Locate every Plasmodium falciparum-infected red blood cell.
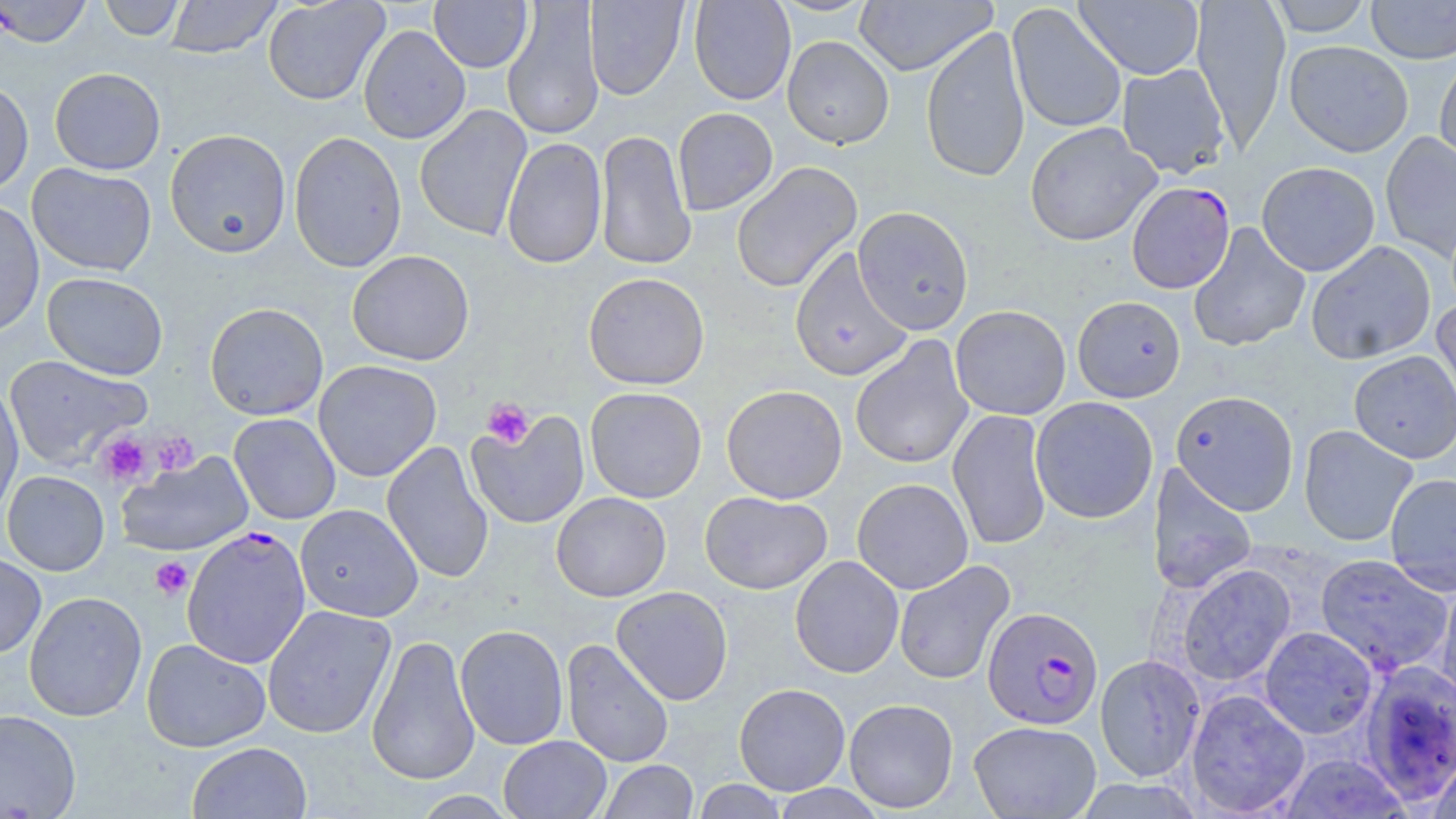
Approximate bounding boxes as (x1,y1)-(x2,y2) corner pairs in pixels.
Plasmodium falciparum-infected red blood cells (subset): (1126,181)-(1235,294), (182,526)-(312,668), (982,606)-(1104,729).

{
  "slide_level_diagnosis": "Plasmodium falciparum",
  "stain": "May-Grünwald-Giemsa",
  "preparation": "thin blood smear",
  "platelet_locations": "approximate bounding boxes as (x1,y1)-(x2,y2) corner pairs in pixels: (483,398)-(534,449), (151,431)-(199,475), (97,432)-(153,487), (149,556)-(193,601)",
  "field_of_view": "single",
  "modality": "optical microscopy",
  "uninfected_red_blood_cell_locations_subset": "approximate bounding boxes as (x1,y1)-(x2,y2) corner pairs in pixels: (99,0)-(185,41), (164,0)-(282,58), (262,0)-(389,106), (429,0)-(533,73), (689,0)-(796,105), (769,0)-(879,17), (853,0)-(997,76), (1074,0)-(1205,80), (1192,0)-(1291,151), (1267,0)-(1373,37), (1365,0)-(1456,63), (501,1)-(605,140), (585,1)-(688,100), (1007,3)-(1127,134), (358,25)-(470,144), (921,26)-(1030,183), (782,36)-(894,149), (1284,40)-(1414,157), (1435,54)-(1456,170), (1116,63)-(1230,179), (49,67)-(166,175), (0,79)-(34,197), (415,104)-(532,242), (673,107)-(778,215), (1024,123)-(1160,246), (165,129)-(291,258), (595,129)-(696,270), (288,131)-(407,273), (1380,131)-(1456,262), (501,137)-(607,269), (1256,161)-(1380,277), (27,162)-(156,276), (731,162)-(863,293), (0,199)-(45,338), (853,206)-(974,335), (1187,222)-(1311,352), (1306,240)-(1436,365), (789,246)-(914,382), (347,250)-(475,366), (42,272)-(168,380), (583,272)-(710,390), (1072,295)-(1186,402), (1431,297)-(1456,426), (204,302)-(329,420), (950,305)-(1071,420), (850,336)-(974,470), (1349,350)-(1456,464), (3,355)-(152,471), (313,360)-(442,482), (0,384)-(23,520), (721,385)-(847,504), (585,387)-(707,503), (1170,390)-(1299,515), (1030,396)-(1158,524), (465,409)-(590,529), (947,409)-(1052,551), (229,413)-(341,524), (1298,424)-(1418,547), (382,441)-(494,584), (116,452)-(254,557), (1147,464)-(1258,596), (1,470)-(110,576), (1384,473)-(1456,595), (852,478)-(973,594), (699,491)-(832,595), (551,492)-(671,602), (295,504)-(422,621), (0,551)-(47,659), (1315,553)-(1455,678), (789,556)-(904,679), (893,560)-(1016,686), (1175,564)-(1296,687), (1434,577)-(1456,711), (611,586)-(733,705), (24,591)-(147,722), (262,605)-(396,738), (455,624)-(569,750), (1259,626)-(1378,738), (367,633)-(480,786), (141,638)-(271,753), (562,638)-(674,768), (1095,654)-(1205,782), (1359,660)-(1455,805), (734,683)-(850,795), (1185,689)-(1310,817), (844,698)-(959,813), (0,708)-(81,818), (968,720)-(1102,818), (499,735)-(611,819), (187,741)-(311,819), (1428,752)-(1456,819), (1274,753)-(1413,818), (598,760)-(699,818), (692,780)-(789,819), (770,784)-(888,818)",
  "image_size": "1456×819 pixels",
  "magnification": "1000x"
}